Identify the parasite.
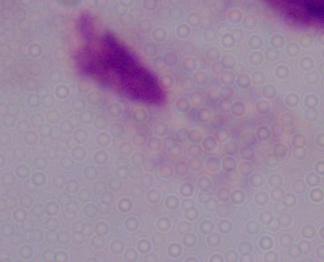

A trichomonad.

modality = photomicrograph
magnification = 1000x